Outline each blood parasite and name the species.
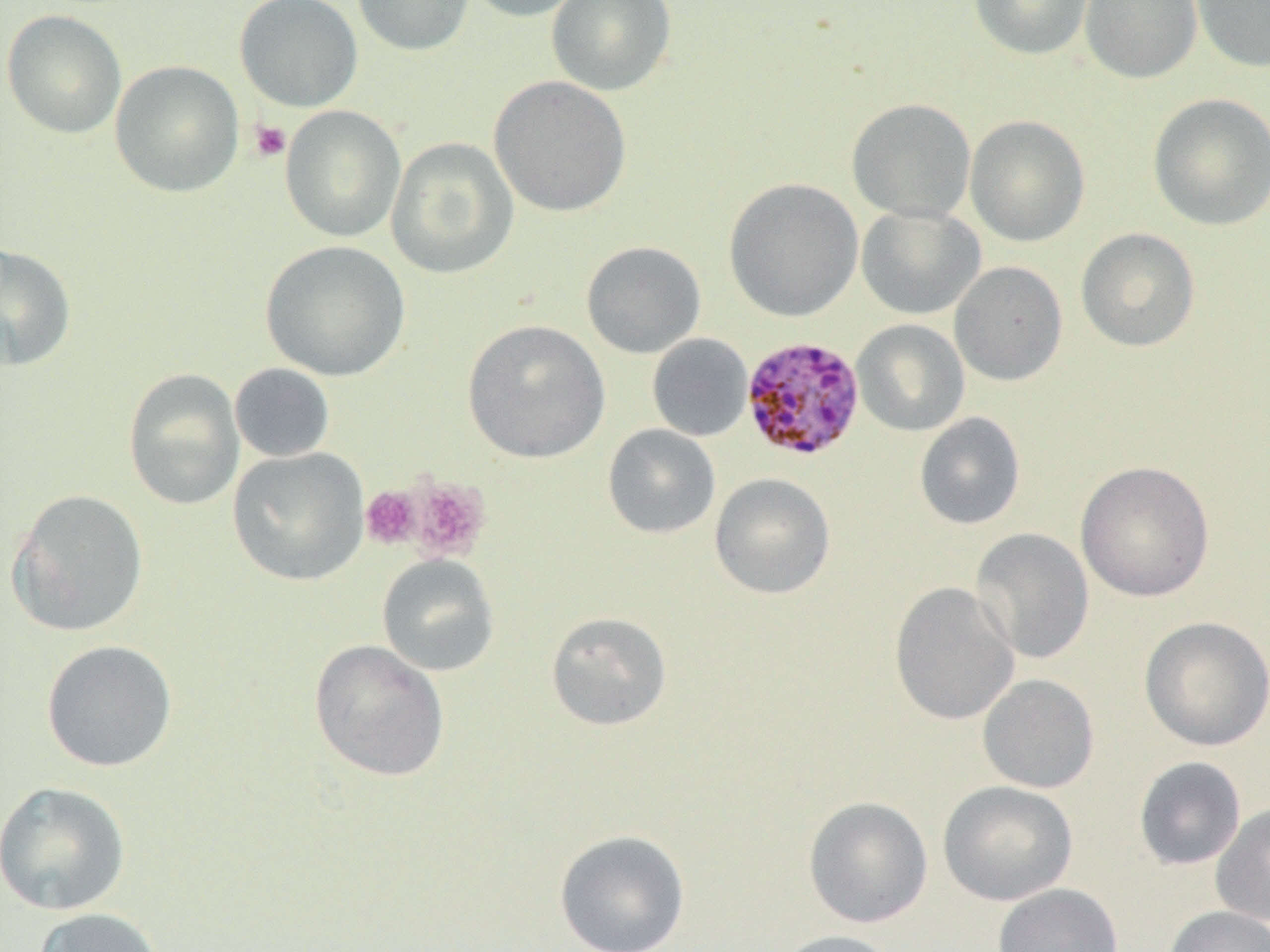
Approximate bounding boxes as [x1, y1, x2, y2] in pixels.
Plasmodium malariae-infected red blood cells: [741, 336, 866, 462].
No Plasmodium falciparum, Plasmodium ovale, Plasmodium vivax, Babesia divergens, or Trypanosoma brucei observed.

Platelet locations: [249, 120, 292, 162], [406, 477, 491, 561], [360, 486, 422, 549]. Uninfected red blood cell locations: [235, 0, 363, 112], [351, 0, 474, 56], [460, 0, 591, 22], [546, 0, 676, 96], [969, 0, 1094, 60], [1080, 0, 1202, 83], [1191, 0, 1270, 72], [1, 10, 127, 139], [110, 60, 244, 197], [489, 75, 632, 218], [1148, 93, 1270, 231], [846, 98, 977, 223], [280, 105, 406, 242], [964, 115, 1090, 247], [386, 136, 519, 280], [723, 177, 864, 321], [856, 204, 985, 320], [1076, 228, 1200, 352], [260, 240, 410, 382], [581, 241, 706, 358], [0, 243, 77, 372], [949, 261, 1068, 386], [462, 319, 611, 463], [852, 320, 970, 436], [647, 333, 753, 441], [230, 363, 335, 463], [123, 368, 245, 510], [914, 412, 1026, 530], [602, 424, 721, 538], [227, 447, 370, 586], [1075, 460, 1215, 602], [709, 473, 836, 600], [6, 489, 149, 637], [970, 528, 1095, 663], [377, 554, 500, 676], [889, 582, 1020, 725], [545, 611, 672, 730], [1139, 616, 1270, 752], [308, 639, 450, 782], [41, 640, 178, 772], [978, 674, 1100, 793], [1134, 756, 1246, 870], [0, 780, 132, 916], [937, 780, 1078, 906], [803, 796, 933, 928], [1211, 802, 1270, 926], [554, 829, 691, 952], [993, 883, 1124, 952], [1162, 905, 1270, 952], [32, 907, 166, 952], [773, 929, 903, 952]. Slide-level diagnosis: Plasmodium malariae. Image is 1270×952 pixels. Light microscopy. Thin blood film. Single field of view. Captured at 1000x magnification.